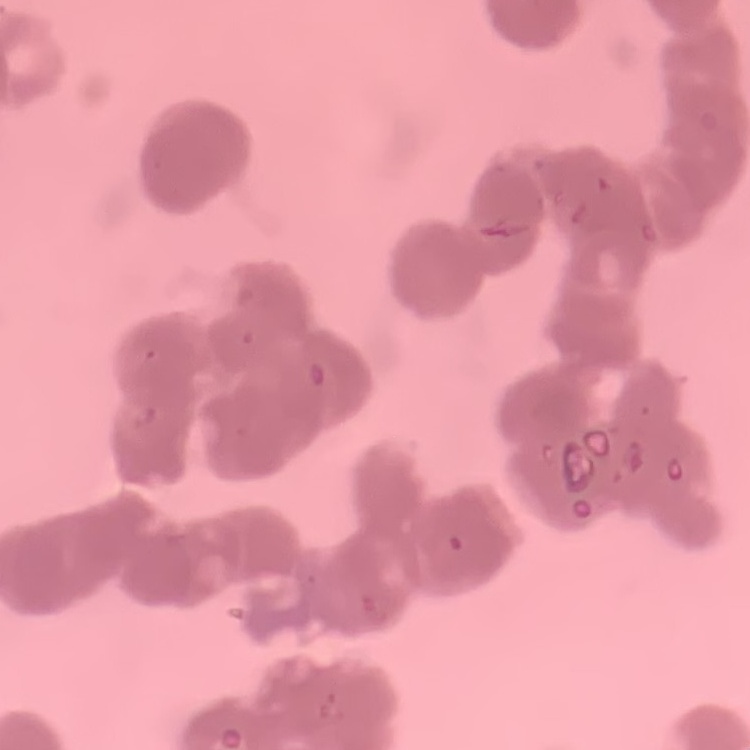

Summary:
  - Red blood cell morphology: rouleaux formation
  - Stain: Field's or Giemsa
  - Preparation: thin blood smear
  - Image type: square crop of a larger photomicrograph